Report the malaria status of this cell.
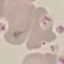
It is uninfected.

Summary:
  - Stain: Giemsa
  - Image type: automatically extracted cell patch, resized to 64 × 64 pixels
  - Preparation: thin blood film
  - Capture: smartphone through the microscope eyepiece